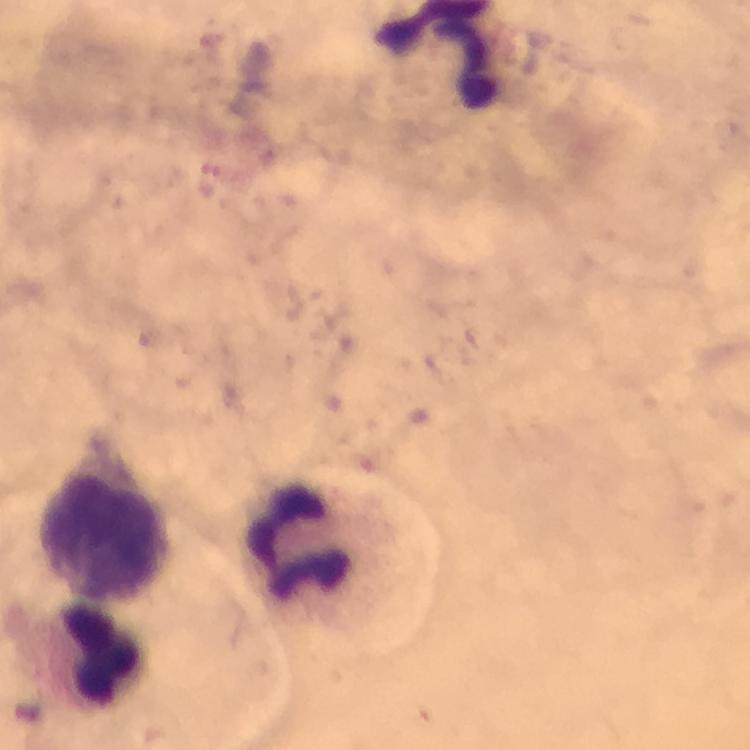 Approximate object centers, in pixels from the top-left corner. Leukocyte locations: (x=106, y=533), (x=297, y=537), (x=97, y=656). Photographed through the microscope with a smartphone camera. Giemsa-stained preparation. From a malaria diagnostic workup. Cropped region of a single field of view. Immersion oil was used. Image is 750×750 pixels. Malaria parasites: none seen. At 100x magnification. Thick blood smear.